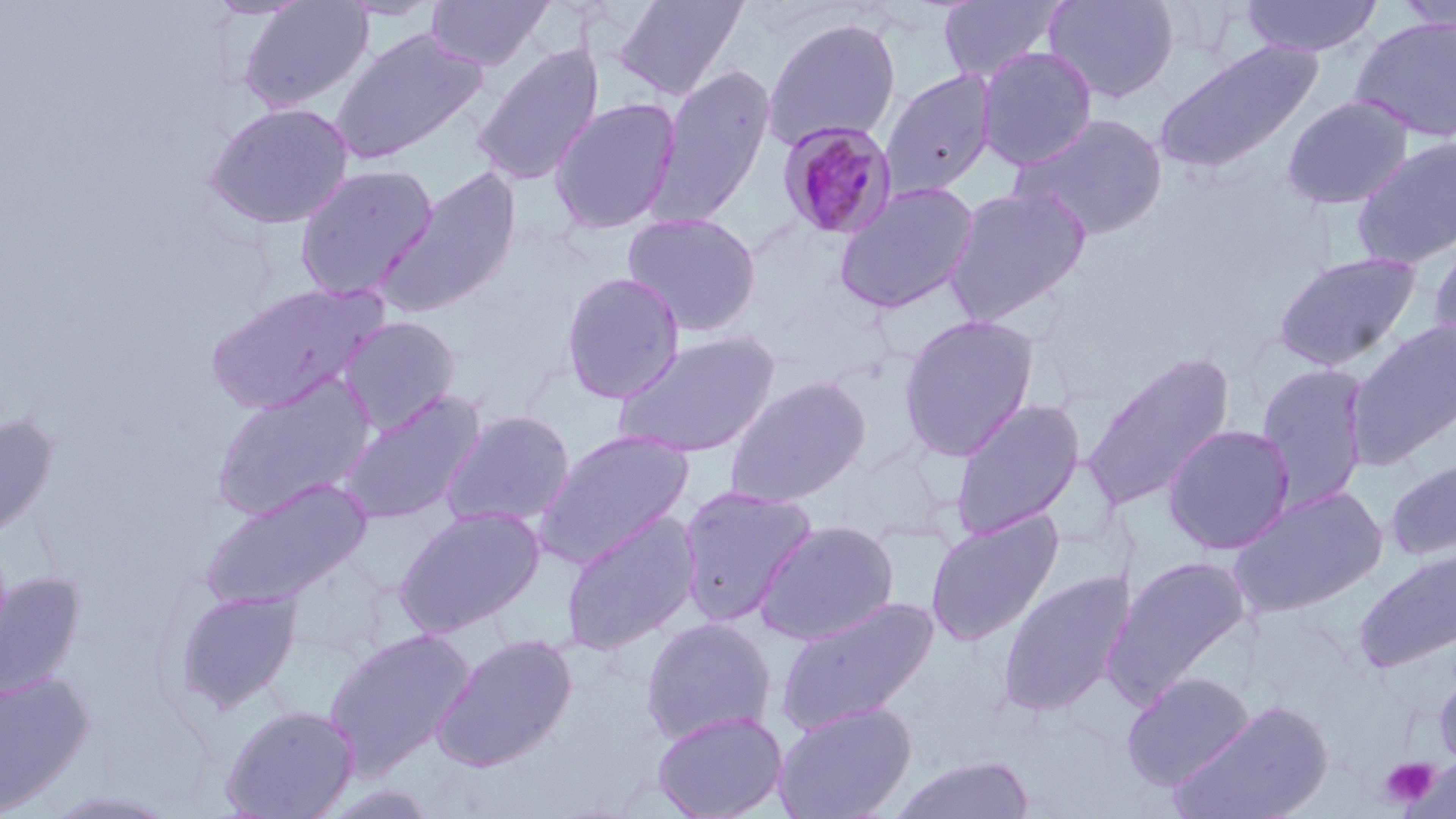
slide-level diagnosis = Plasmodium malariae
field of view = single
stain = May-Grünwald-Giemsa
image size = 1456×819 pixels
modality = optical microscopy
Plasmodium malariae-infected red blood cell locations = approximate bounding boxes as (x1,y1)-(x2,y2) corner pairs in pixels: (776,120)-(900,241)
platelet locations = approximate bounding boxes as (x1,y1)-(x2,y2) corner pairs in pixels: (1380,756)-(1440,809)
preparation = thin blood smear
magnification = 1000x
uninfected red blood cell locations = approximate bounding boxes as (x1,y1)-(x2,y2) corner pairs in pixels: (205,0)-(312,20), (238,0)-(373,113), (337,0)-(443,21), (425,0)-(553,70), (613,0)-(749,100), (937,0)-(1064,83), (1043,0)-(1180,104), (1240,0)-(1382,58), (1396,1)-(1456,36), (762,17)-(902,151), (1350,17)-(1456,143), (331,27)-(487,165), (1152,39)-(1324,176), (472,44)-(604,187), (976,47)-(1097,171), (649,64)-(776,230), (881,70)-(996,199), (1282,94)-(1414,210), (549,98)-(681,235), (204,101)-(355,230), (1011,112)-(1169,241), (1350,136)-(1456,269), (294,164)-(439,301), (376,167)-(523,318), (833,181)-(980,315), (943,184)-(1090,327), (622,211)-(762,336), (1426,238)-(1456,361), (1272,250)-(1422,373), (560,271)-(685,404), (202,281)-(388,415), (899,315)-(1039,460), (337,316)-(461,434), (1346,320)-(1456,470), (612,329)-(781,459), (1081,351)-(1236,511), (1256,363)-(1371,512), (724,375)-(871,508), (212,376)-(376,520), (337,389)-(487,527), (949,399)-(1085,539), (441,410)-(576,529), (0,412)-(59,539), (1163,423)-(1296,555), (534,430)-(694,567), (1384,457)-(1456,562), (198,477)-(372,610), (677,484)-(818,626), (1227,485)-(1387,618), (395,507)-(544,637), (560,510)-(702,655), (925,510)-(1064,647), (754,519)-(900,646), (1354,548)-(1456,674), (1102,555)-(1252,706), (997,569)-(1136,717), (0,571)-(84,703), (173,589)-(303,714), (776,595)-(939,735), (640,617)-(777,745), (323,627)-(476,776), (432,634)-(578,772), (0,670)-(95,814), (1120,671)-(1255,790), (1433,671)-(1456,772), (773,700)-(917,819), (1167,701)-(1334,819), (220,705)-(359,818), (651,710)-(788,819), (890,754)-(1036,818), (40,790)-(182,819)